Give the extent of all uninfected red blood cells.
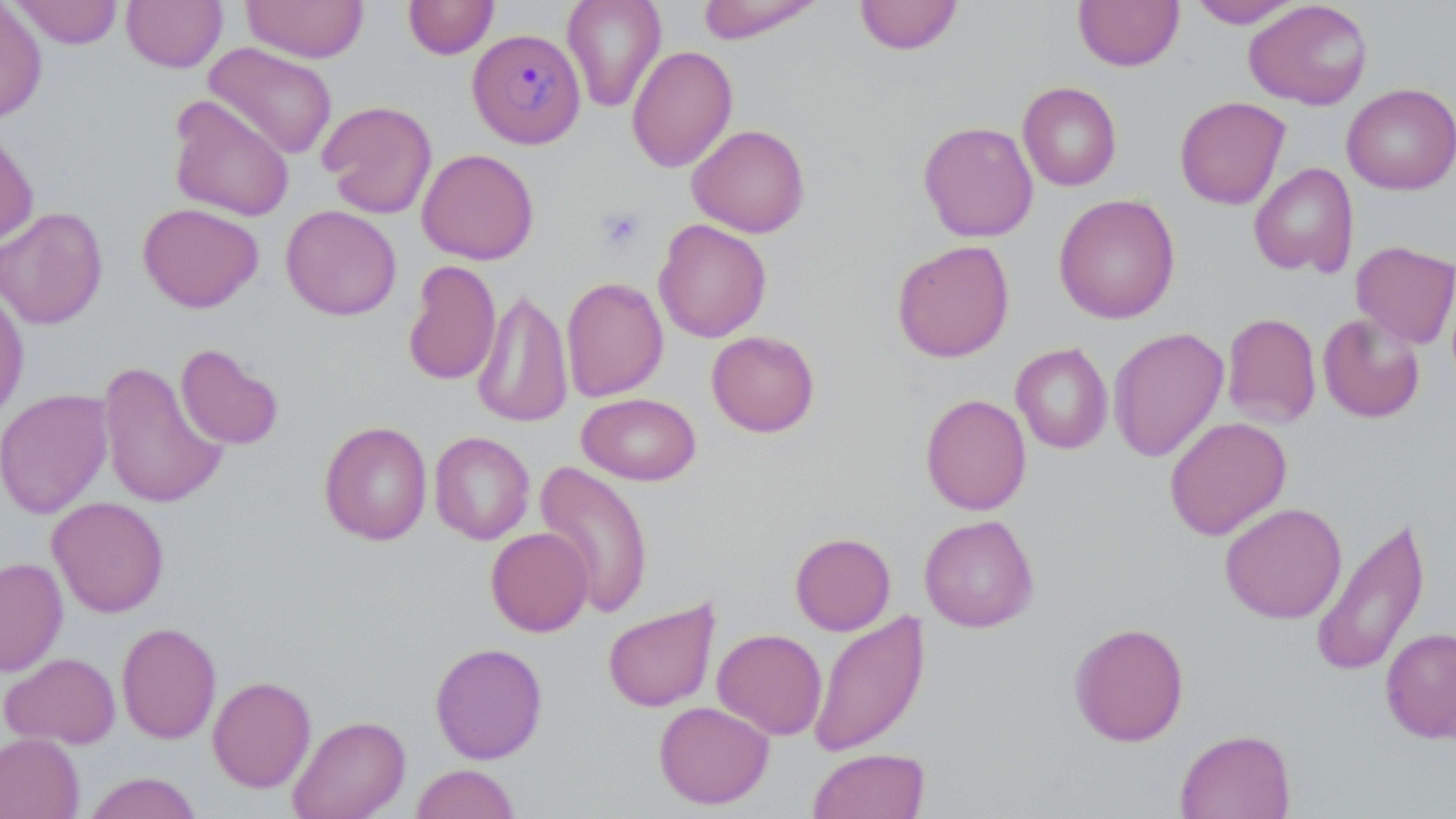
Approximate bounding boxes as [x1, y1, x2, y2] in pixels.
Uninfected red blood cells: [9, 0, 124, 48], [121, 0, 228, 73], [242, 0, 369, 63], [402, 0, 499, 59], [562, 0, 667, 113], [697, 0, 826, 44], [853, 0, 965, 55], [1187, 0, 1303, 28], [1072, 1, 1185, 71], [1244, 1, 1373, 110], [0, 2, 47, 125], [203, 42, 339, 161], [626, 45, 738, 173], [1018, 81, 1122, 191], [1341, 83, 1456, 195], [168, 95, 295, 222], [1174, 96, 1291, 209], [317, 100, 438, 219], [918, 121, 1038, 242], [687, 123, 811, 238], [0, 125, 39, 249], [416, 148, 539, 265], [1249, 162, 1359, 278], [1053, 193, 1181, 324], [138, 202, 264, 313], [280, 205, 402, 321], [0, 206, 108, 330], [654, 218, 772, 343], [891, 239, 1015, 362], [1351, 240, 1456, 349], [402, 259, 501, 387], [561, 276, 668, 402], [0, 286, 29, 424], [471, 287, 573, 428], [1317, 311, 1426, 424], [1221, 312, 1321, 429], [1108, 326, 1229, 462], [706, 330, 820, 437], [175, 343, 284, 451], [1011, 343, 1113, 454], [97, 360, 228, 509], [0, 389, 114, 519], [577, 392, 701, 486], [920, 394, 1032, 515], [1164, 416, 1292, 540], [318, 421, 433, 546], [429, 431, 535, 544], [534, 460, 654, 619], [47, 496, 169, 617], [1219, 503, 1347, 624], [919, 514, 1039, 633], [1310, 514, 1431, 679], [486, 527, 594, 637], [789, 532, 896, 635], [0, 556, 68, 676], [602, 598, 721, 713], [808, 610, 930, 758], [1069, 621, 1189, 747], [116, 622, 221, 744], [1380, 627, 1456, 743], [713, 628, 827, 740], [429, 642, 548, 764], [0, 652, 121, 749], [207, 675, 316, 793], [653, 700, 774, 809], [288, 714, 411, 819], [1175, 728, 1296, 819], [0, 732, 84, 819], [809, 748, 930, 819], [410, 763, 521, 819], [82, 771, 203, 819].

Platelet locations: [596, 208, 645, 252]. Plasmodium malariae-infected red blood cell locations: [467, 28, 586, 148]. Slide-level diagnosis: Plasmodium malariae. Image is 1456×819 pixels. Single field of view. May-Grünwald-Giemsa-stained preparation. Light microscopy. Thin blood smear. Captured at 1000x magnification.